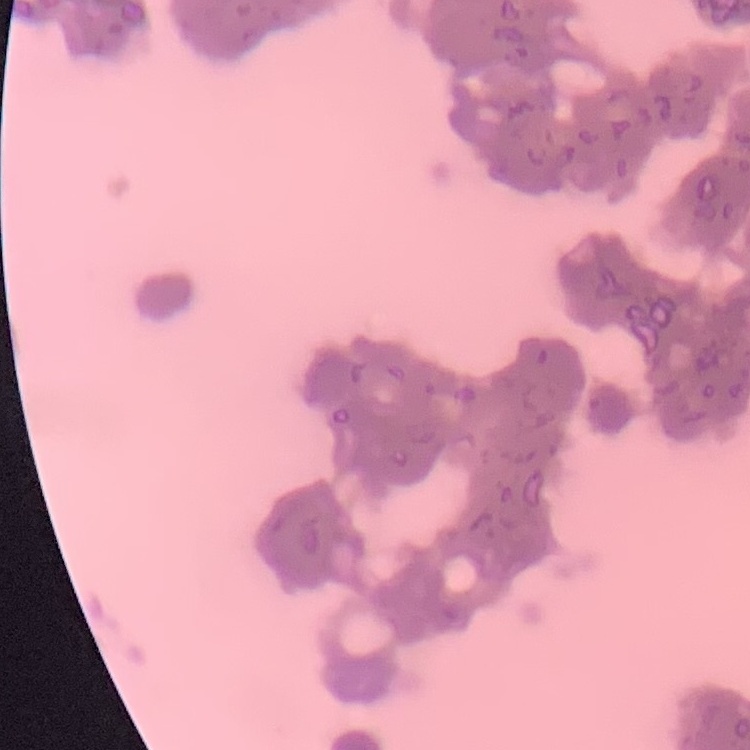

The erythrocytes show rouleaux formation. Square crop of a larger photomicrograph. Stained with either Field's or Giemsa. Thin blood film.